Mark where platelets are.
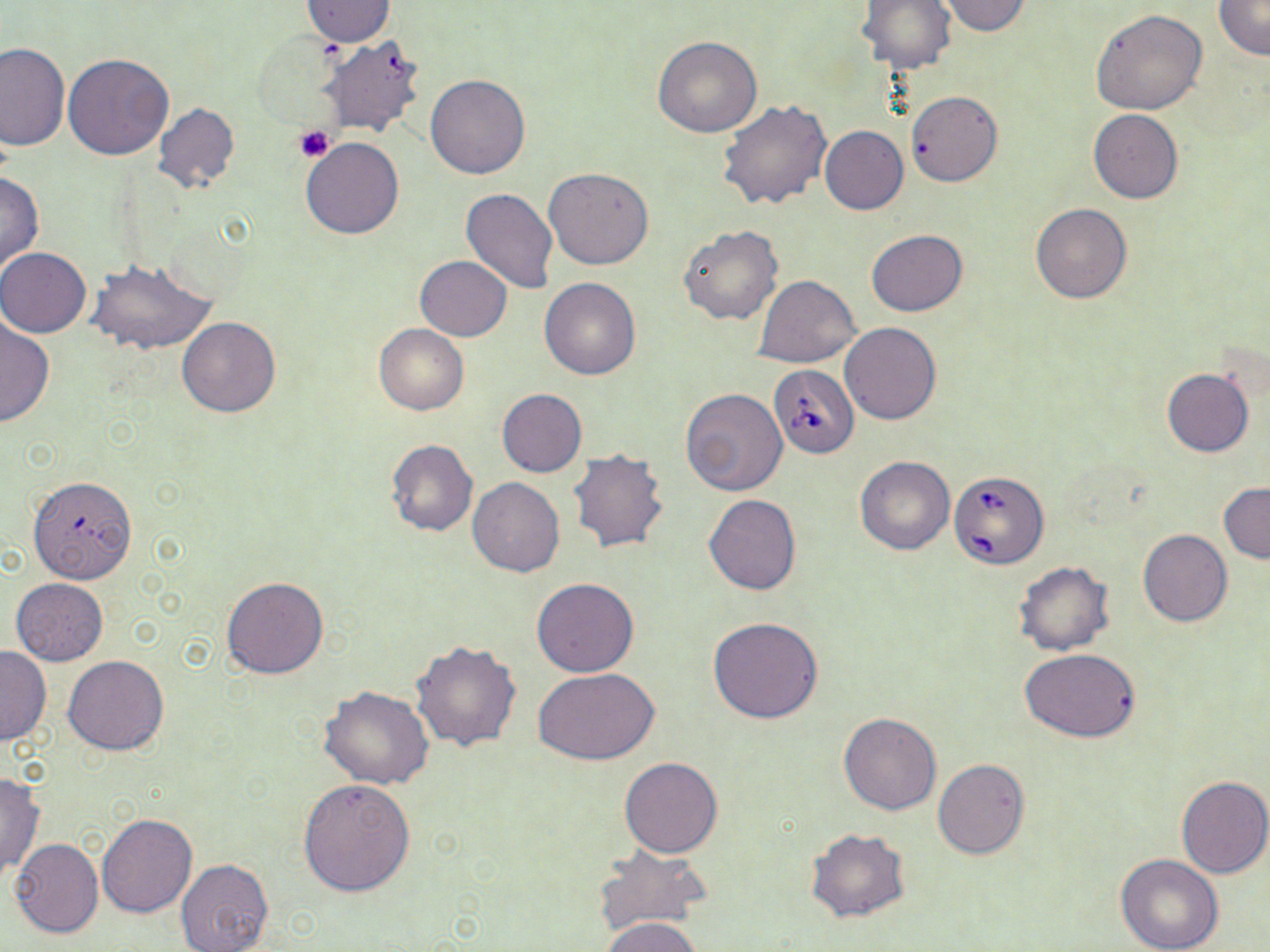

Approximate bounding boxes as (x1, y1, x2, y2) in pixels.
Platelets: (295, 125, 335, 162).

slide-level diagnosis = Babesia divergens
preparation = thin blood smear
stain = May-Grünwald-Giemsa
uninfected red blood cell locations = approximate bounding boxes as (x1, y1, x2, y2) in pixels: (864, 0, 957, 73), (1214, 0, 1270, 60), (302, 1, 394, 46), (936, 1, 1032, 35), (1091, 8, 1208, 115), (318, 35, 426, 136), (653, 37, 761, 137), (0, 42, 69, 152), (64, 53, 174, 160), (424, 73, 530, 180), (907, 90, 1003, 186), (717, 99, 830, 210), (152, 102, 240, 194), (1088, 108, 1182, 204), (819, 125, 908, 214), (301, 137, 404, 239), (544, 167, 653, 269), (0, 170, 44, 276), (461, 188, 558, 293), (1030, 203, 1132, 304), (679, 225, 783, 324), (866, 230, 968, 316), (0, 247, 91, 337), (415, 256, 511, 341), (84, 258, 217, 357), (754, 274, 859, 367), (539, 277, 642, 380), (177, 317, 280, 417), (0, 318, 54, 428), (840, 322, 942, 425), (375, 325, 468, 414), (1162, 368, 1255, 457), (681, 388, 787, 495), (496, 389, 587, 477), (385, 439, 478, 537), (567, 449, 670, 554), (854, 456, 955, 555), (27, 476, 138, 584), (467, 478, 564, 576), (1219, 483, 1270, 562), (704, 494, 801, 594), (1139, 529, 1233, 626), (1013, 560, 1116, 656), (220, 577, 329, 679), (11, 579, 108, 666), (531, 579, 638, 677), (708, 615, 825, 724), (411, 639, 521, 751), (0, 646, 51, 745), (1020, 649, 1142, 741), (63, 655, 169, 754), (533, 668, 660, 766), (319, 687, 434, 790), (838, 712, 941, 814), (619, 756, 722, 857), (932, 758, 1029, 859), (0, 772, 45, 885), (1176, 776, 1270, 879), (297, 778, 416, 895), (96, 813, 198, 917), (806, 828, 911, 924), (11, 838, 104, 939), (595, 842, 714, 935), (1115, 852, 1224, 952), (175, 858, 272, 952), (602, 917, 703, 952)
field of view = single
image size = 1270×952 pixels
modality = light microscopy
magnification = 1000x
Babesia divergens-infected red blood cell locations = approximate bounding boxes as (x1, y1, x2, y2) in pixels: (770, 364, 858, 457), (950, 469, 1050, 570)